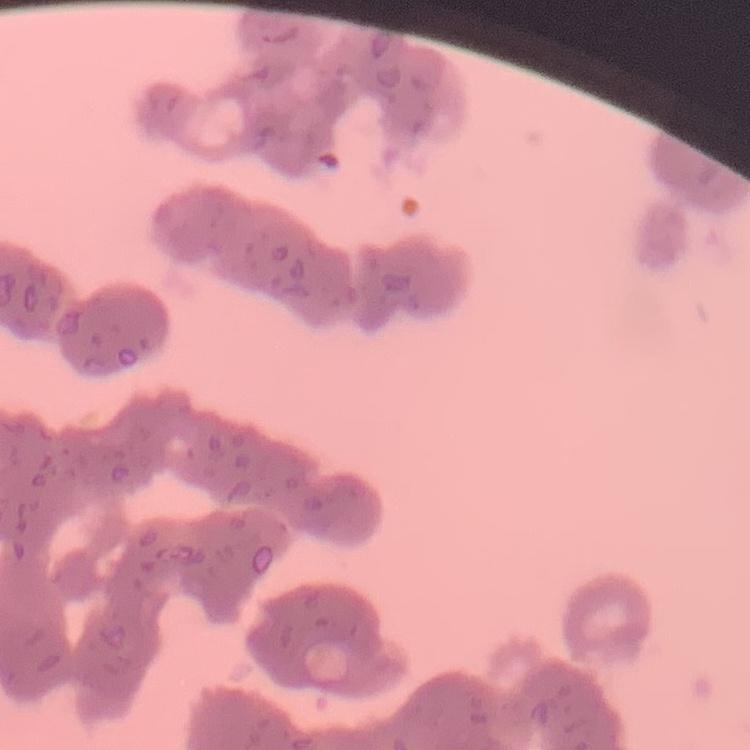
red blood cell morphology = rouleaux formation
preparation = thin blood smear
stain = Field's or Giemsa
image type = square crop of a larger photomicrograph